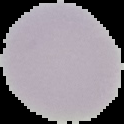
image type = cell region segmented out of the field of view; surrounding area masked to black
preparation = thin blood film
image size = 124×124 pixels
result = no malaria parasites detected